Name the cell type shown.
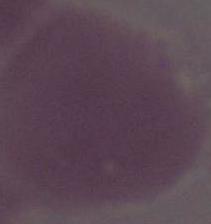

An erythrocyte.

Micrograph. Captured at 1000x magnification.